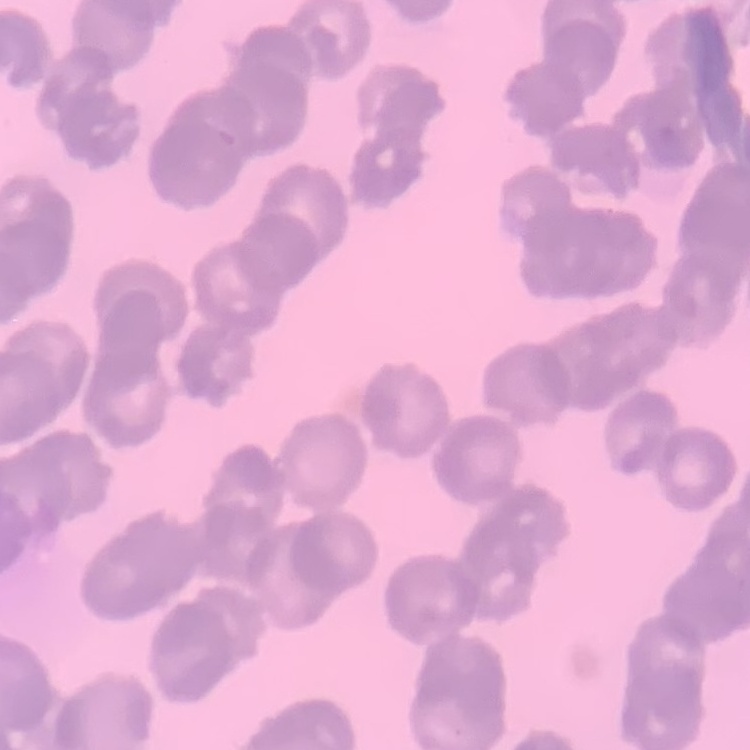
The erythrocytes exhibit rouleaux formation. Stained with either Field's or Giemsa. Square crop of a larger photomicrograph. Thin blood film.